Locate every Plasmodium parasite.
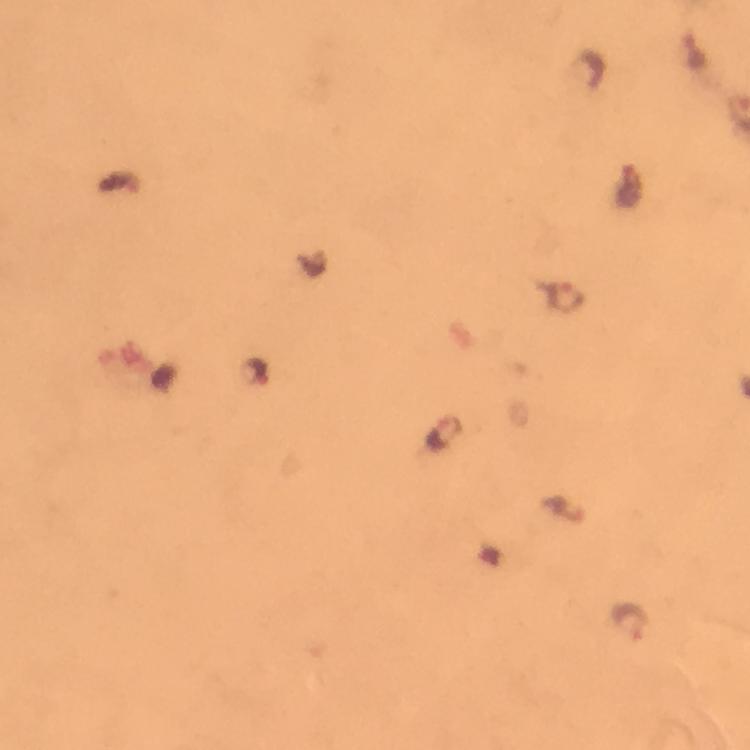
Approximate centers as (x, y) in pixels.
Plasmodium parasites: (696, 53), (630, 188), (569, 297), (445, 430), (630, 622).

magnification: 100x
stain: Giemsa
preparation: thick blood film
immersion_oil: applied
capture: smartphone mounted on the microscope
image_size: 750×750 pixels
context: from a malaria diagnostic workup
cropped_from: a single field of view